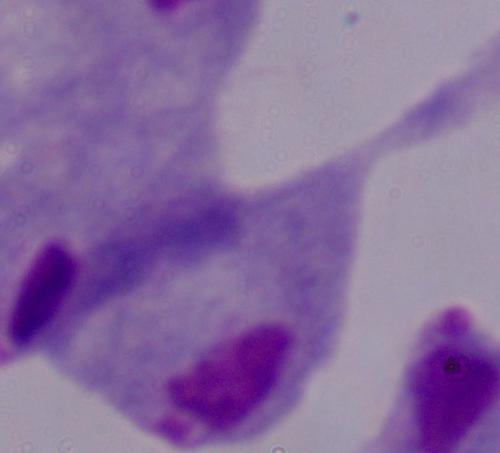
Summary:
  - Magnification: 1000x
  - Identification: trichomonad
  - Modality: micrograph